Assess this cell for malaria.
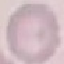

It is uninfected.

{
  "image_type": "automatically extracted cell patch, resized to 64 × 64 pixels",
  "preparation": "thin blood smear",
  "capture": "smartphone through the microscope eyepiece",
  "stain": "Giemsa"
}